Name the cell type shown.
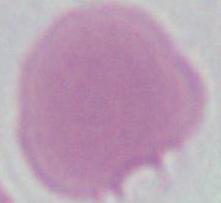

An erythrocyte.

{
  "modality": "micrograph",
  "magnification": "1000x"
}